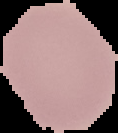

Summary:
  - Result: negative for malaria parasites
  - Image size: 118×133 pixels
  - Image type: segmented cell region with the area outside set to black
  - Preparation: thin blood film